Identify the parasite.
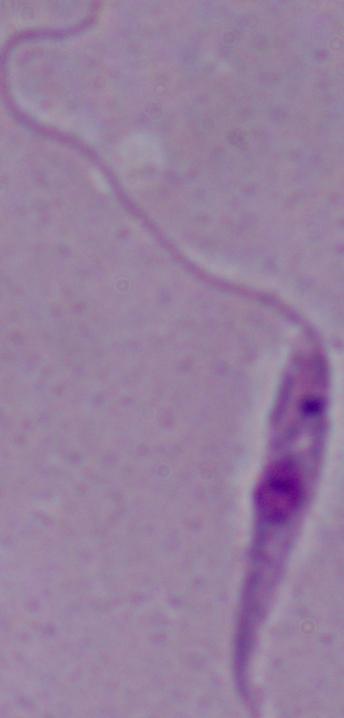

Leishmania.

{
  "modality": "micrograph",
  "magnification": "1000x"
}